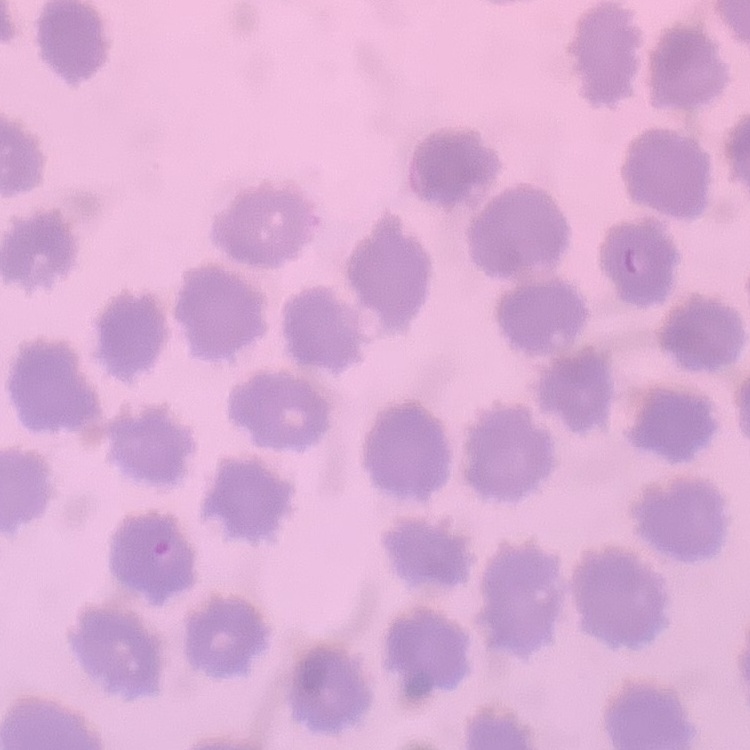
{
  "erythrocyte_morphology": "no rouleaux formation",
  "preparation": "thin peripheral smear",
  "stain": "Field's or Giemsa",
  "image_type": "square crop of a larger photomicrograph"
}